Report the malaria status of this cell.
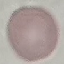

It is uninfected.

Thin smear of blood. Giemsa stain. Automatically extracted cell patch, resized to 64 × 64 pixels. Photographed with a smartphone camera at the microscope eyepiece.